State which cell type is depicted.
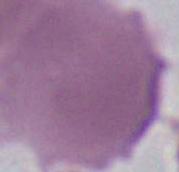
An erythrocyte.

modality = micrograph
magnification = 1000x